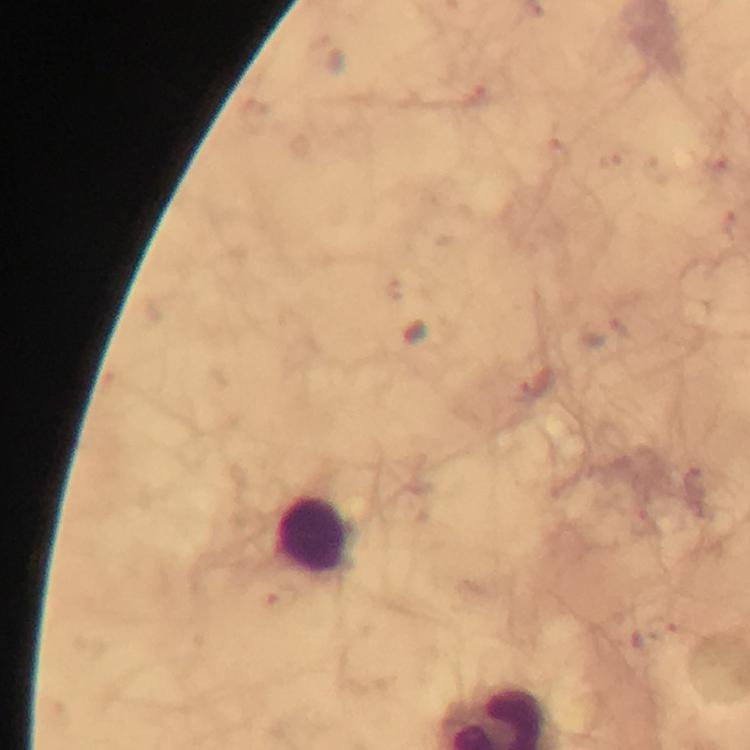

Approximate centers as [x, y] in pixels.
Summary:
  - Leukocyte locations: [316, 534]
  - Stain: Giemsa
  - Immersion oil: applied
  - Preparation: thick blood film
  - Cropped from: one field of view
  - Context: from a malaria diagnostic workup
  - Capture: smartphone camera through the microscope
  - Image size: 750×750 pixels
  - Malaria parasites: none seen
  - Magnification: 100x